Locate every leukocyte (white blood cell).
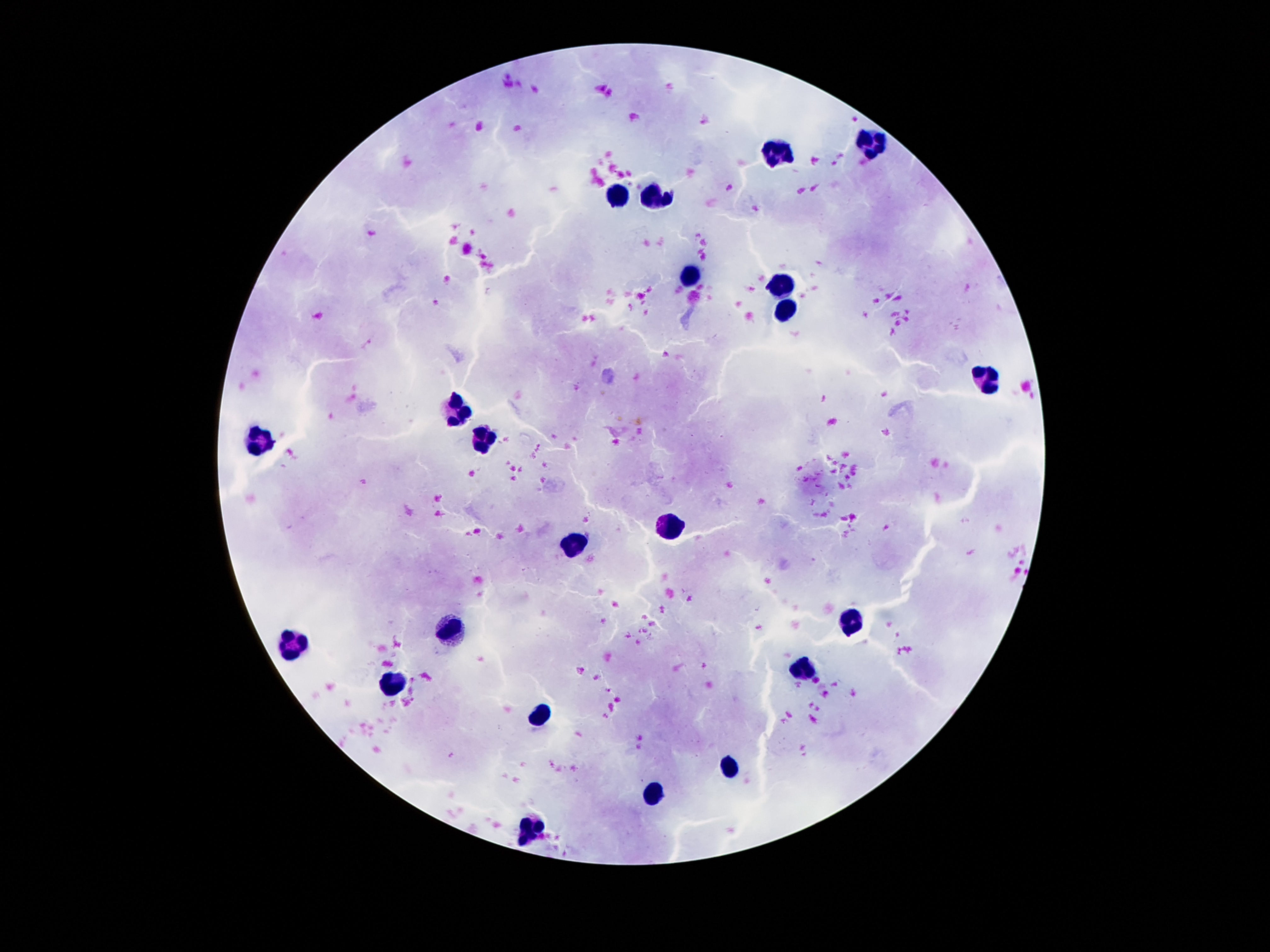

Approximate centers as {x, y} in pixels.
Leukocytes: {875, 142}, {778, 152}, {656, 194}, {621, 196}, {688, 278}, {778, 288}, {785, 307}, {983, 377}, {457, 405}, {477, 437}, {263, 443}, {670, 525}, {572, 543}, {851, 619}, {451, 631}, {291, 642}, {804, 668}, {399, 684}, {543, 715}, {729, 767}, {655, 799}, {531, 828}.

patient_malaria_status: uninfected
magnification: 100x
capture: smartphone camera through the microscope eyepiece
field_of_view: single
image_size: 1270×952 pixels
stain: Giemsa
preparation: thick blood smear